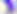
Captured at 400x magnification. Micrograph. Toxoplasma gondii is seen.